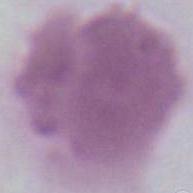

An erythrocyte is seen. 1000x magnification. Photomicrograph.